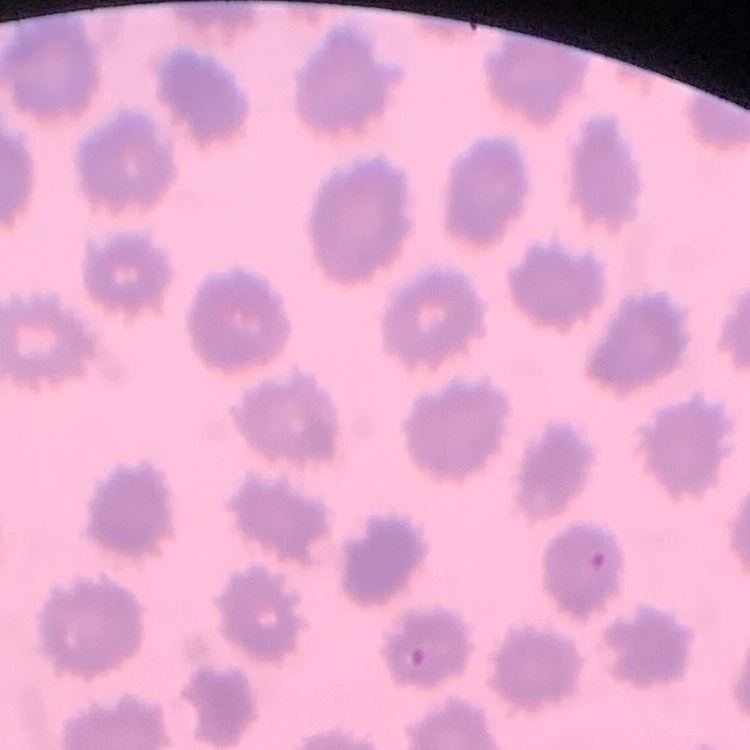

Summary:
  - Red blood cell morphology: no rouleaux formation
  - Image type: square crop of a larger photomicrograph
  - Stain: Field's or Giemsa
  - Preparation: thin blood film